Report the malaria status of this cell.
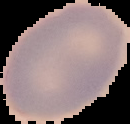

It is uninfected.

preparation = thin blood smear
image type = cell region segmented out of the field of view; surrounding area masked to black
image size = 130×124 pixels